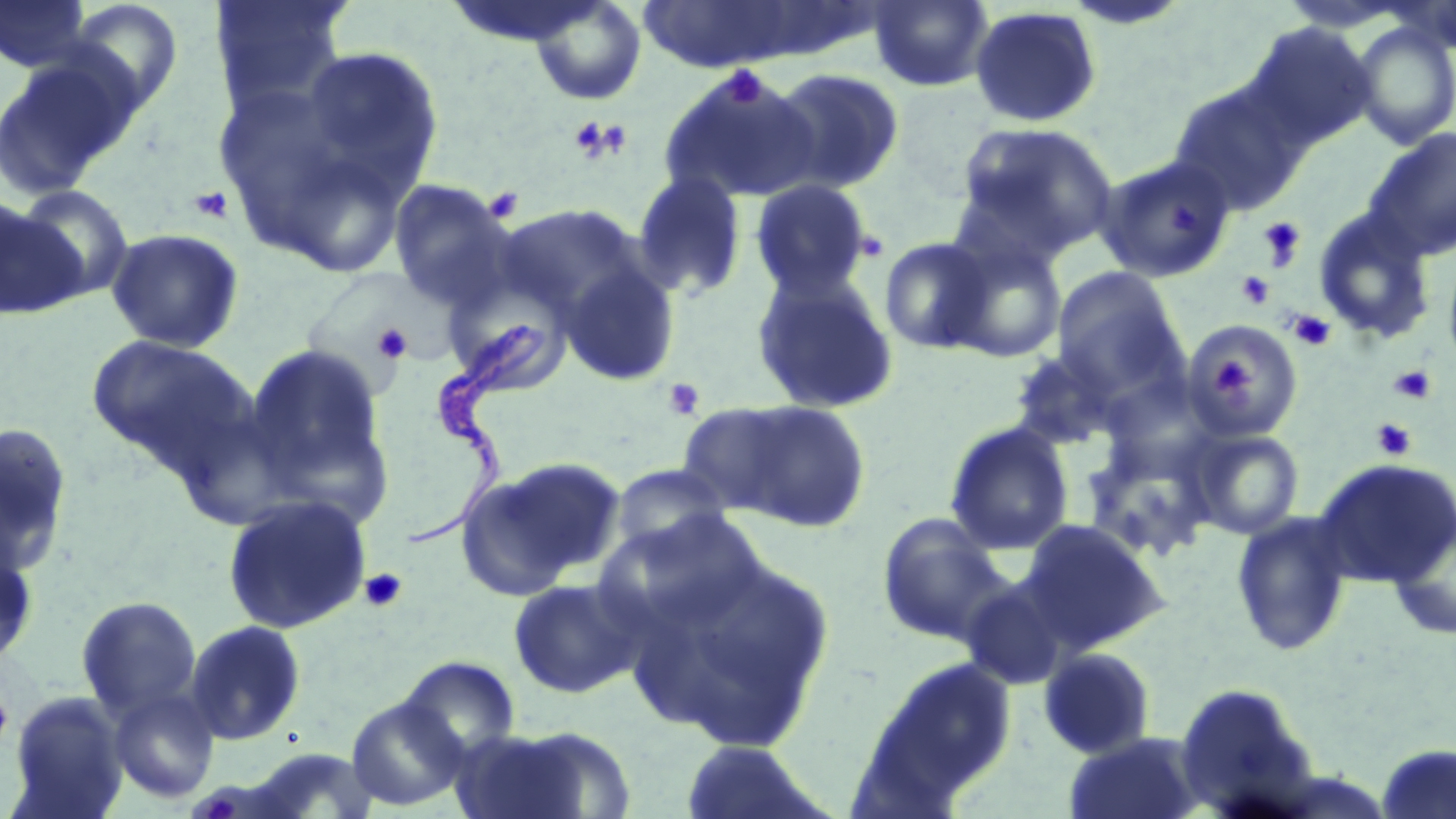
Summary:
  - Coordinate format: approximate bounding boxes as named x1/y1/x2/y2 corners in pixels
  - Uninfected red blood cell locations: (x1=0, y1=0, x2=95, y2=73), (x1=57, y1=0, x2=185, y2=117), (x1=208, y1=0, x2=353, y2=122), (x1=868, y1=0, x2=995, y2=93), (x1=529, y1=1, x2=647, y2=105), (x1=630, y1=1, x2=817, y2=73), (x1=969, y1=5, x2=1102, y2=128), (x1=1242, y1=22, x2=1377, y2=151), (x1=1351, y1=22, x2=1456, y2=150), (x1=295, y1=44, x2=444, y2=198), (x1=0, y1=53, x2=141, y2=199), (x1=767, y1=67, x2=906, y2=193), (x1=659, y1=68, x2=822, y2=206), (x1=1168, y1=84, x2=1307, y2=214), (x1=955, y1=121, x2=1119, y2=262), (x1=1362, y1=127, x2=1456, y2=262), (x1=1095, y1=154, x2=1236, y2=283), (x1=631, y1=171, x2=749, y2=301), (x1=386, y1=179, x2=519, y2=311), (x1=748, y1=179, x2=875, y2=300), (x1=14, y1=184, x2=135, y2=304), (x1=1, y1=199, x2=80, y2=318), (x1=497, y1=203, x2=649, y2=325), (x1=1312, y1=207, x2=1438, y2=345), (x1=106, y1=227, x2=244, y2=353), (x1=878, y1=235, x2=997, y2=355), (x1=943, y1=235, x2=1069, y2=363), (x1=1441, y1=247, x2=1456, y2=378), (x1=557, y1=258, x2=681, y2=386), (x1=1051, y1=266, x2=1187, y2=398), (x1=749, y1=268, x2=901, y2=415), (x1=442, y1=275, x2=575, y2=398), (x1=1184, y1=320, x2=1305, y2=440), (x1=85, y1=333, x2=253, y2=469), (x1=241, y1=341, x2=394, y2=516), (x1=1006, y1=346, x2=1137, y2=451), (x1=713, y1=398, x2=873, y2=533), (x1=674, y1=401, x2=811, y2=519), (x1=943, y1=421, x2=1075, y2=554), (x1=0, y1=423, x2=74, y2=576), (x1=1185, y1=426, x2=1305, y2=540), (x1=456, y1=456, x2=626, y2=600), (x1=1312, y1=457, x2=1456, y2=588), (x1=609, y1=464, x2=734, y2=559), (x1=221, y1=495, x2=372, y2=634), (x1=597, y1=508, x2=773, y2=644), (x1=1229, y1=511, x2=1355, y2=658), (x1=875, y1=513, x2=1015, y2=648), (x1=1386, y1=513, x2=1456, y2=642), (x1=1018, y1=519, x2=1170, y2=652), (x1=0, y1=530, x2=40, y2=669), (x1=630, y1=550, x2=837, y2=751), (x1=507, y1=577, x2=645, y2=699), (x1=75, y1=596, x2=203, y2=721), (x1=184, y1=620, x2=306, y2=746), (x1=1037, y1=646, x2=1158, y2=760), (x1=396, y1=654, x2=523, y2=761), (x1=878, y1=656, x2=1018, y2=795), (x1=1173, y1=682, x2=1318, y2=813), (x1=107, y1=685, x2=220, y2=804), (x1=8, y1=692, x2=129, y2=817), (x1=346, y1=695, x2=470, y2=811), (x1=463, y1=724, x2=635, y2=818), (x1=1065, y1=731, x2=1207, y2=819), (x1=678, y1=738, x2=832, y2=819), (x1=1375, y1=744, x2=1456, y2=817), (x1=245, y1=747, x2=380, y2=818)
  - Platelet locations: (x1=718, y1=65, x2=770, y2=109), (x1=567, y1=114, x2=630, y2=165), (x1=483, y1=186, x2=524, y2=223), (x1=189, y1=187, x2=234, y2=224), (x1=1257, y1=216, x2=1307, y2=271), (x1=1235, y1=271, x2=1275, y2=310), (x1=1288, y1=310, x2=1336, y2=352), (x1=370, y1=323, x2=412, y2=365), (x1=1208, y1=357, x2=1250, y2=400), (x1=1388, y1=365, x2=1437, y2=405), (x1=662, y1=378, x2=706, y2=421), (x1=1370, y1=418, x2=1417, y2=461), (x1=358, y1=567, x2=408, y2=612), (x1=0, y1=685, x2=14, y2=750)
  - Trypanosoma brucei locations: (x1=405, y1=323, x2=545, y2=549)
  - Slide-level diagnosis: Trypanosoma brucei
  - Image size: 1456×819 pixels
  - Modality: optical microscopy
  - Magnification: 1000x
  - Stain: May-Grünwald-Giemsa
  - Preparation: thin blood film
  - Field of view: single